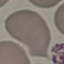

result = no malaria parasites detected
image type = automatically extracted cell patch, resized to 64 × 64 pixels
stain = Giemsa
preparation = thin blood film
capture = smartphone camera at the microscope eyepiece